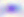 Toxoplasma gondii is shown. Captured at 400x magnification. Micrograph.